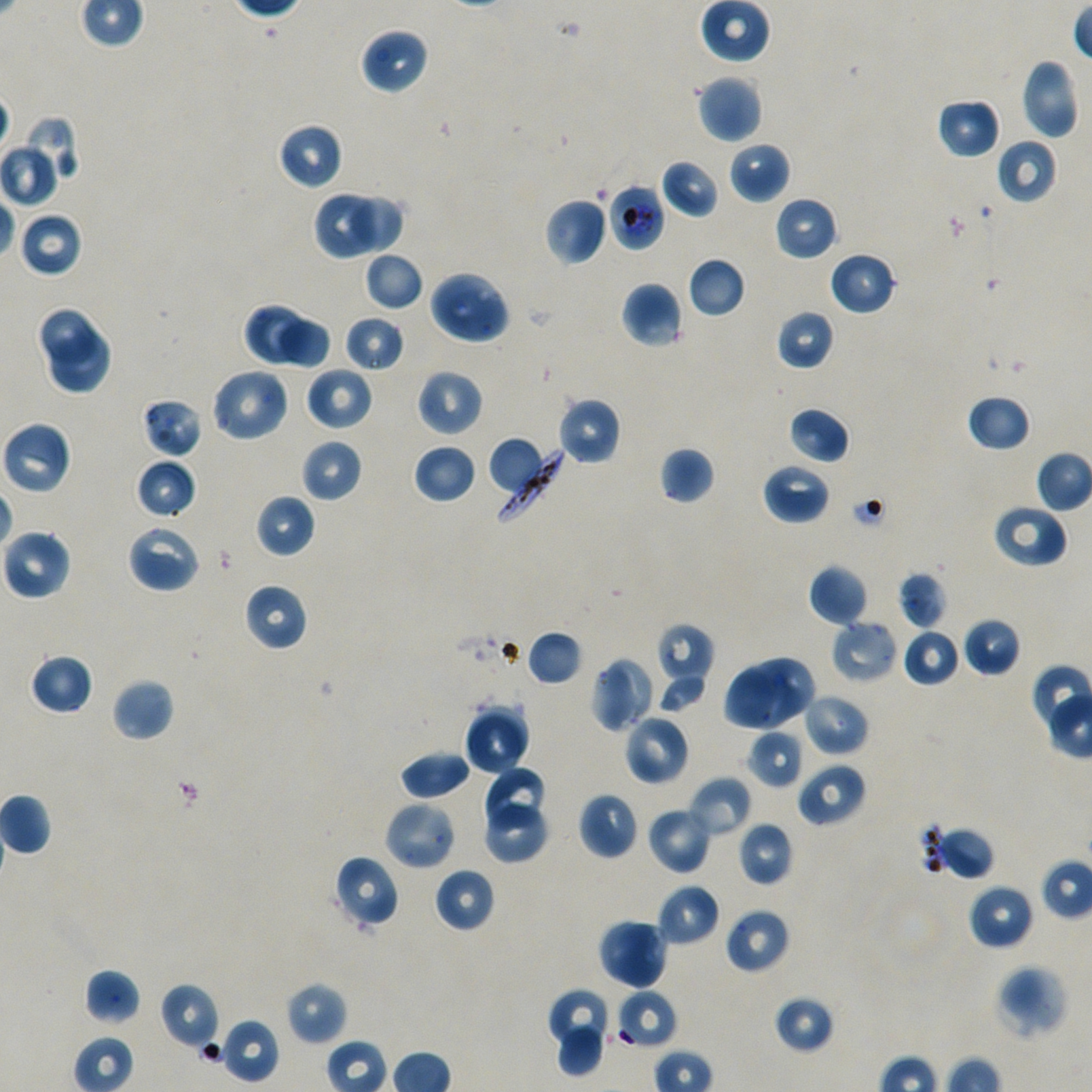
Approximate bounding boxes as {x1, y1, x2, y2} in pixels. Not every red blood cell is marked.
Summary:
  - Locations of red blood cells of indeterminate infection status: {608, 183, 666, 252}, {616, 989, 677, 1049}
  - Locations of uninfected red blood cells: {699, 0, 771, 63}, {359, 26, 429, 95}, {1019, 56, 1080, 141}, {696, 75, 763, 143}, {936, 97, 1001, 159}, {21, 113, 81, 187}, {276, 122, 344, 191}, {996, 139, 1057, 204}, {0, 141, 61, 208}, {729, 141, 790, 204}, {660, 158, 721, 219}, {313, 190, 377, 261}, {349, 193, 407, 253}, {774, 196, 838, 261}, {545, 197, 608, 266}, {18, 211, 84, 278}, {363, 251, 424, 312}, {829, 251, 897, 316}, {687, 257, 746, 318}, {428, 269, 512, 346}, {621, 280, 684, 348}, {242, 303, 304, 366}, {37, 306, 98, 366}, {776, 308, 835, 370}, {344, 315, 405, 374}, {276, 316, 331, 371}, {46, 330, 114, 396}, {304, 366, 374, 431}, {210, 367, 291, 443}, {416, 368, 484, 437}, {966, 394, 1032, 452}, {556, 396, 622, 466}, {141, 397, 203, 459}, {787, 406, 850, 464}, {1, 420, 72, 496}, {487, 437, 543, 492}, {300, 438, 363, 503}, {413, 443, 477, 505}, {658, 446, 715, 505}, {134, 458, 196, 520}, {762, 462, 831, 524}, {255, 494, 316, 558}, {991, 503, 1068, 569}, {126, 524, 201, 594}, {1, 528, 71, 600}, {808, 563, 869, 626}, {898, 570, 947, 630}, {243, 582, 309, 651}, {962, 617, 1021, 677}, {829, 619, 898, 685}, {655, 622, 714, 692}, {902, 629, 962, 687}, {526, 630, 583, 686}, {30, 653, 94, 715}, {755, 655, 818, 721}, {591, 657, 637, 733}, {723, 666, 785, 729}, {657, 670, 709, 712}, {111, 678, 175, 742}, {744, 682, 803, 731}, {801, 693, 869, 757}, {464, 706, 530, 774}, {623, 714, 690, 786}, {747, 728, 805, 788}, {399, 750, 472, 801}, {796, 762, 867, 827}, {481, 766, 547, 826}, {689, 776, 751, 837}, {578, 791, 638, 860}, {383, 800, 457, 871}, {481, 803, 550, 864}, {646, 806, 712, 875}, {738, 821, 793, 887}, {942, 824, 996, 881}, {332, 854, 399, 930}, {434, 867, 496, 933}, {656, 884, 721, 947}, {968, 884, 1034, 950}, {724, 907, 790, 975}, {597, 917, 652, 982}, {619, 923, 667, 991}, {994, 964, 1069, 1040}, {84, 968, 140, 1025}, {286, 981, 348, 1045}, {160, 982, 221, 1050}, {547, 987, 611, 1049}, {773, 994, 836, 1054}, {220, 1019, 279, 1084}, {556, 1023, 605, 1077}
  - Locations of infected red blood cells: {495, 448, 566, 522}
  - Objective: 100x, oil immersion, numerical aperture 1.45
  - Field of view: one from this slide
  - Preparation: thin blood film
  - Donor blood group: A+/O+
  - Culture: P. falciparum strain NF54, static, in vitro
  - Stain: Giemsa
  - Image size: 1092×1092 pixels